Comment on the morphology of the erythrocytes.
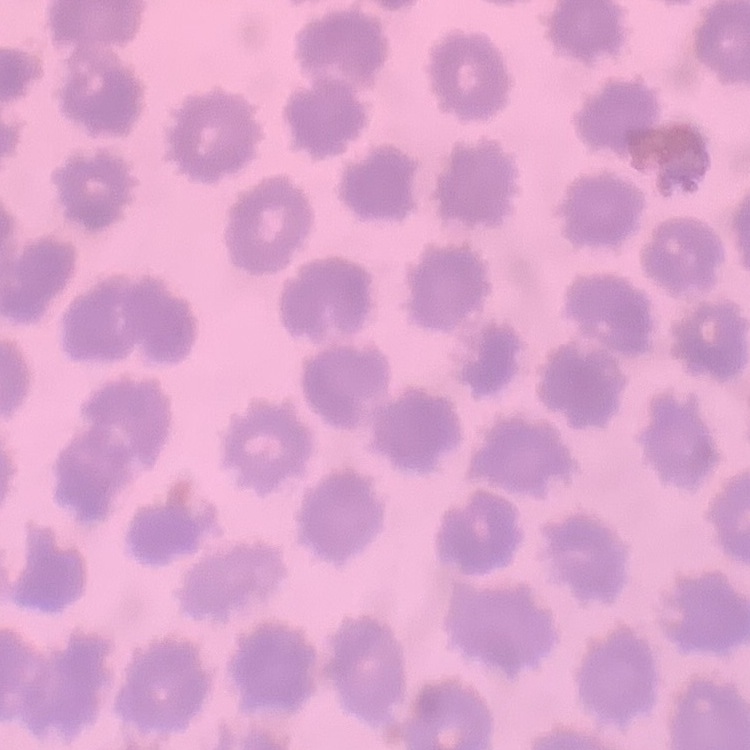

No rouleaux formation.

Summary:
  - Stain: Field's or Giemsa
  - Image type: one tile cut from a larger photomicrograph
  - Preparation: thin blood film